Describe the morphology of the red blood cells.
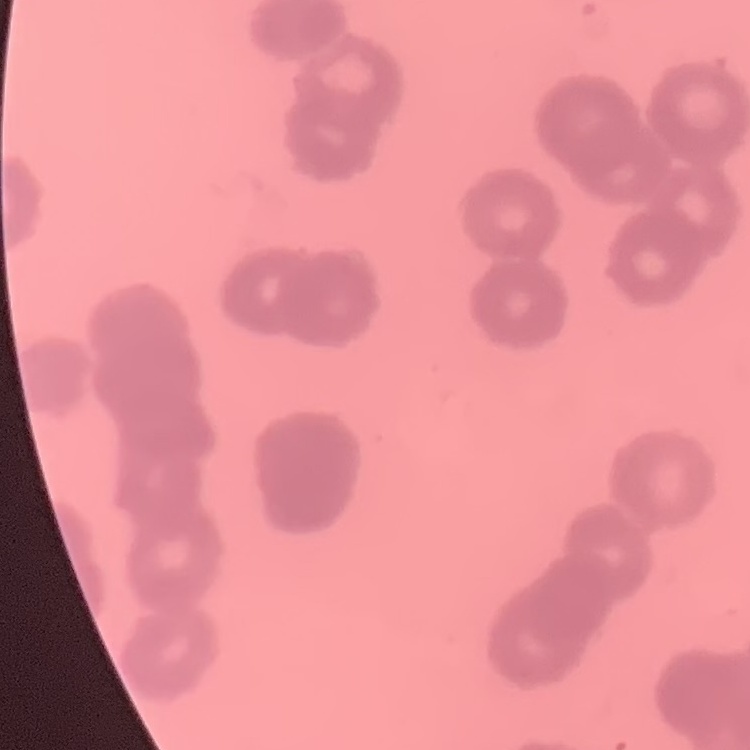

Rouleaux formation.

Summary:
  - Image type: one tile cut from a larger photomicrograph
  - Preparation: thin blood smear
  - Stain: Field's or Giemsa